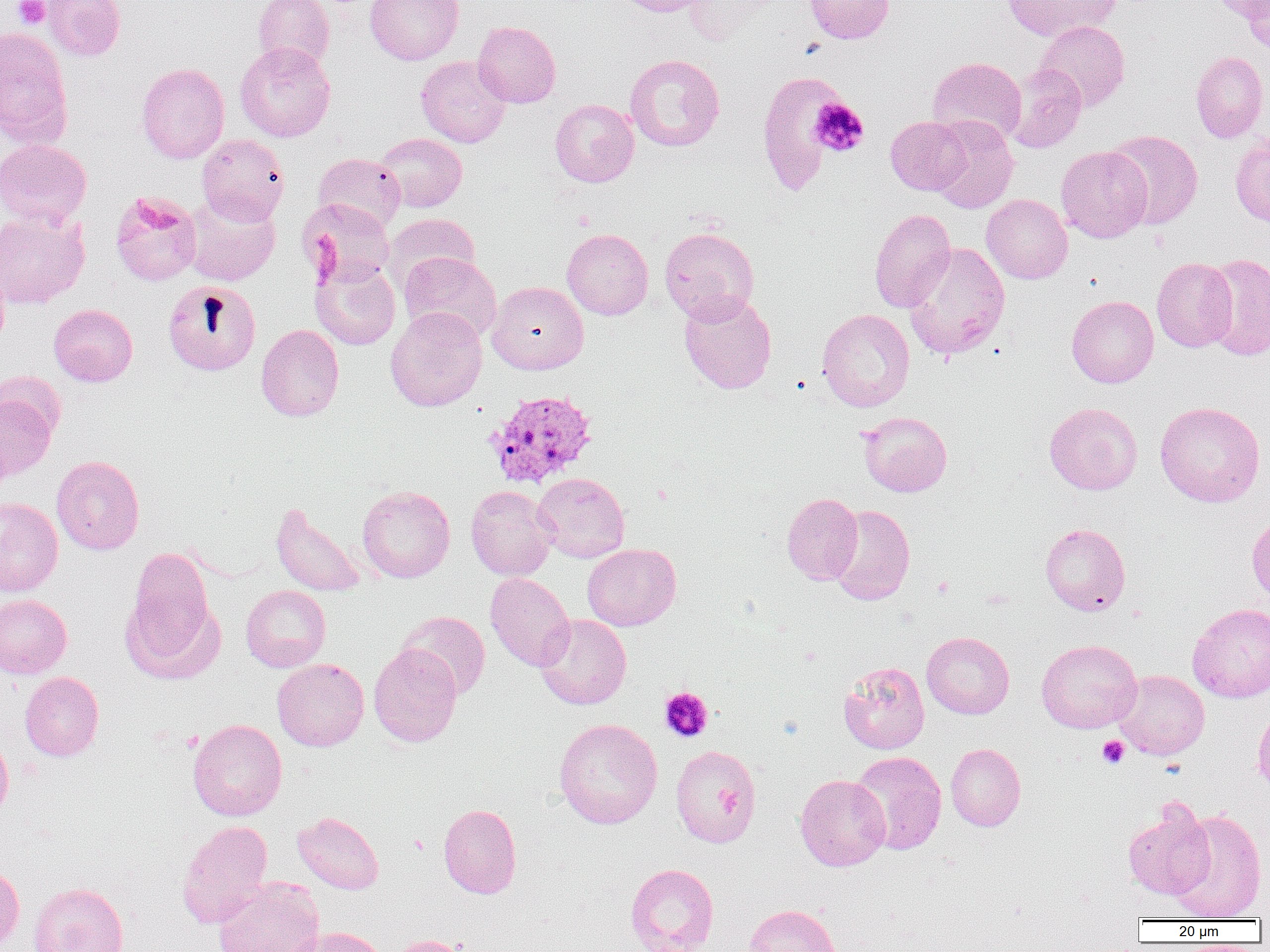
slide-level diagnosis = Plasmodium vivax
field of view = single
magnification = 1000x
Plasmodium vivax-infected red blood cell locations = approximate bounding boxes as (x1, y1, x2, y2) in pixels: (484, 389, 599, 489)
preparation = thin blood smear
image size = 1270×952 pixels
platelet locations = approximate bounding boxes as (x1, y1, x2, y2) in pixels: (13, 0, 49, 29), (809, 97, 869, 157), (659, 687, 713, 742), (1097, 735, 1129, 769), (407, 834, 430, 856)
modality = light microscopy
uninfected red blood cell locations = approximate bounding boxes as (x1, y1, x2, y2) in pixels: (42, 0, 126, 60), (253, 0, 335, 72), (365, 0, 464, 65), (612, 0, 714, 16), (684, 0, 775, 45), (803, 0, 895, 44), (1001, 0, 1121, 42), (1209, 0, 1269, 22), (1240, 1, 1270, 55), (1036, 20, 1130, 111), (473, 21, 561, 108), (0, 27, 72, 145), (234, 41, 335, 142), (1191, 51, 1268, 142), (624, 54, 725, 152), (415, 55, 513, 148), (927, 57, 1027, 146), (136, 62, 230, 164), (1005, 63, 1087, 153), (756, 70, 854, 196), (550, 99, 639, 187), (886, 116, 972, 195), (928, 117, 1019, 214), (1106, 129, 1203, 229), (376, 133, 467, 212), (1230, 133, 1270, 229), (197, 134, 289, 222), (0, 139, 91, 228), (1056, 146, 1153, 243), (314, 153, 406, 232), (110, 190, 202, 286), (183, 192, 281, 286), (981, 194, 1073, 284), (297, 198, 395, 287), (0, 209, 90, 309), (869, 209, 955, 313), (382, 213, 480, 293), (659, 227, 759, 323), (561, 228, 653, 320), (903, 242, 1011, 360), (399, 252, 502, 343), (1203, 253, 1270, 360), (1152, 257, 1238, 352), (311, 260, 400, 350), (0, 262, 10, 353), (163, 279, 261, 376), (487, 281, 589, 375), (678, 292, 777, 393), (1067, 295, 1159, 388), (49, 304, 137, 386), (385, 307, 487, 411), (817, 308, 915, 412), (256, 324, 344, 421), (0, 371, 66, 445), (0, 392, 58, 481), (1155, 401, 1265, 507), (1044, 402, 1142, 495), (858, 411, 952, 496), (52, 456, 145, 555), (532, 473, 630, 562), (357, 485, 455, 583), (466, 485, 557, 580), (781, 493, 863, 584), (0, 498, 63, 596), (270, 501, 367, 597), (828, 504, 915, 605), (1247, 512, 1270, 603), (1040, 523, 1130, 616), (582, 543, 681, 631), (124, 552, 218, 676), (485, 572, 574, 671), (241, 585, 331, 672), (0, 594, 72, 679), (1187, 603, 1270, 702), (396, 611, 491, 700), (534, 614, 632, 710), (921, 632, 1014, 719), (1036, 639, 1142, 733), (368, 644, 462, 747), (272, 659, 369, 751), (838, 661, 930, 754), (1114, 669, 1210, 760), (19, 671, 104, 761), (1253, 704, 1270, 797), (553, 718, 663, 829), (188, 719, 287, 820), (0, 731, 14, 821), (945, 743, 1026, 832), (670, 745, 761, 848), (850, 751, 947, 854), (795, 774, 890, 871), (1122, 799, 1215, 900), (438, 803, 522, 899), (1167, 808, 1266, 921), (292, 811, 384, 894), (177, 820, 273, 928), (0, 862, 25, 950), (625, 863, 719, 951), (213, 877, 324, 952), (28, 881, 128, 952), (743, 903, 841, 952), (290, 926, 388, 952), (388, 934, 474, 952)